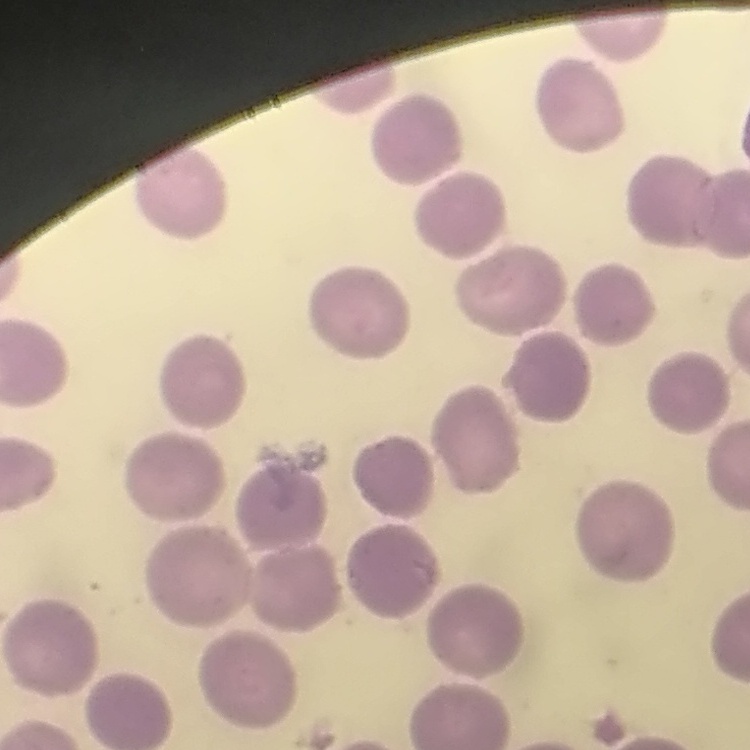

Summary:
  - Red blood cell morphology: no rouleaux formation
  - Preparation: thin blood smear
  - Stain: Field's or Giemsa
  - Image type: one tile cut from a larger photomicrograph